Look for Plasmodium parasites.
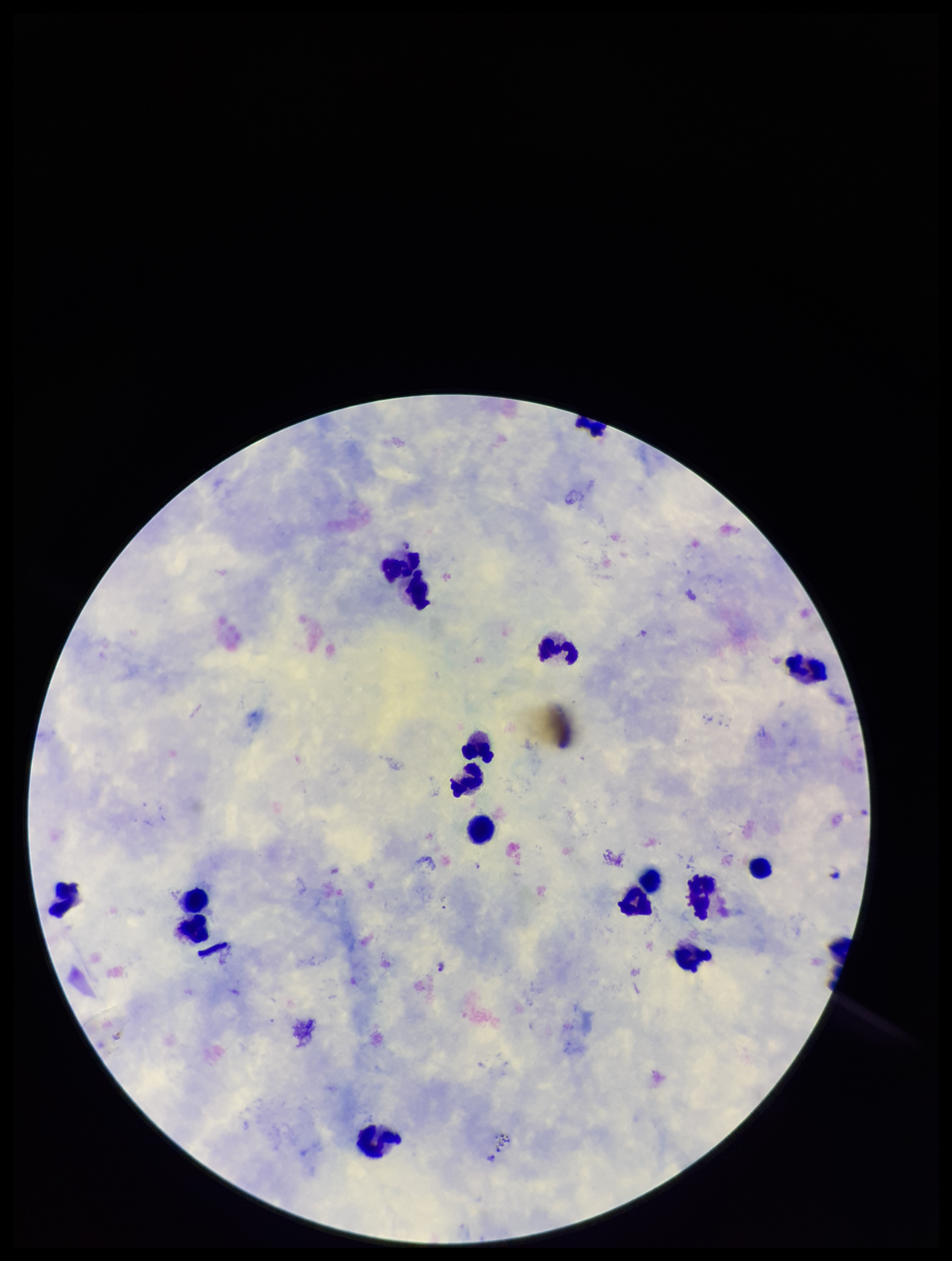
Identified.

Leukocyte count: 16. Photographed through the microscope eyepiece with a smartphone camera. Image is 952×1261 pixels. Giemsa stain. Single field of view. Parasite count: 1. Species reported for this patient: Plasmodium falciparum. Preparation: thick. Patient malaria status: positive.